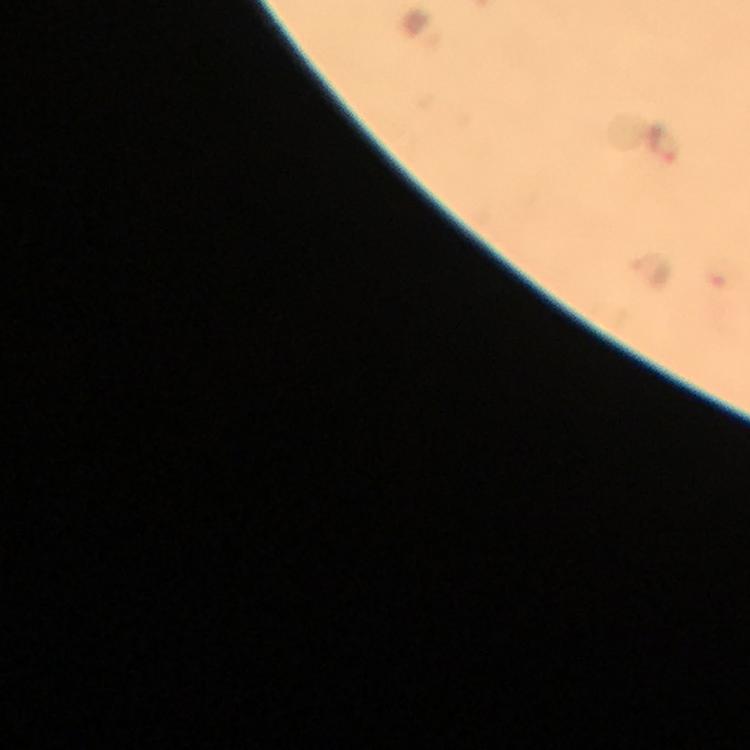

Approximate centers as [x, y] in pixels. Plasmodium parasite locations: [663, 144], [653, 265]. Photographed through the microscope with a smartphone camera. Cropped region of a single field of view. Image is 750×750 pixels. From a diagnostic examination for malaria. Thick smear. Immersion oil applied. Giemsa-stained preparation. 100x magnification.